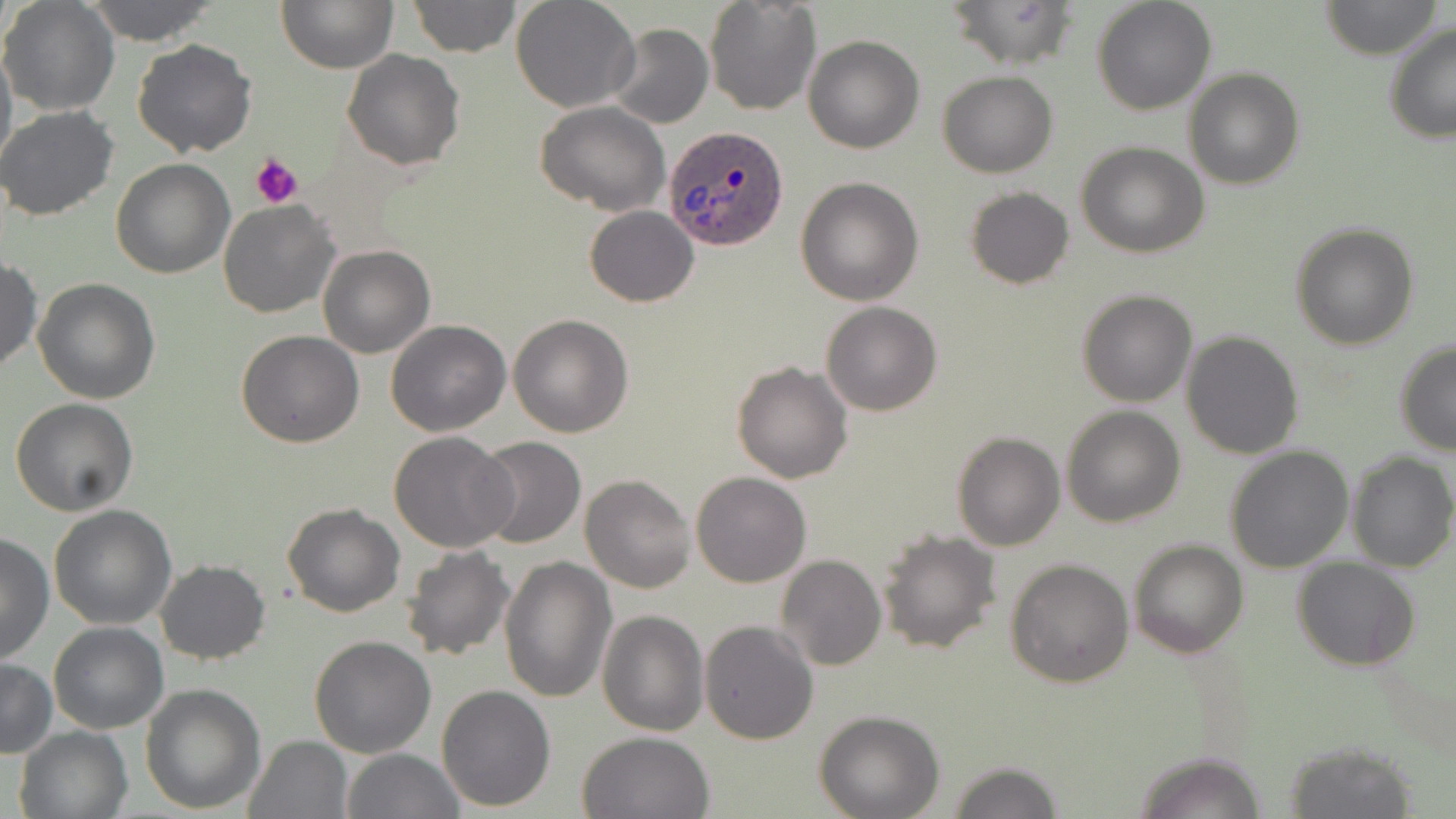
Approximate bounding boxes as (x1,y1)-(x2,y2) corner pairs in pixels. Plasmodium ovale-infected red blood cell locations: (663,123)-(790,250). Uninfected red blood cell locations: (1,0)-(120,117), (83,0)-(220,46), (279,0)-(397,72), (510,0)-(639,113), (704,0)-(822,117), (945,0)-(1079,71), (1091,0)-(1216,115), (407,1)-(521,57), (1321,1)-(1443,58), (1384,21)-(1456,144), (605,23)-(713,129), (0,34)-(16,174), (804,35)-(925,154), (132,38)-(256,156), (342,49)-(466,170), (1183,68)-(1304,189), (938,70)-(1056,177), (536,101)-(670,214), (0,106)-(121,221), (1076,141)-(1209,257), (110,157)-(234,278), (795,176)-(925,305), (965,187)-(1073,290), (219,200)-(339,318), (584,206)-(699,307), (1290,223)-(1420,350), (317,245)-(435,359), (0,255)-(42,372), (32,278)-(160,405), (1077,288)-(1198,406), (821,301)-(942,416), (508,314)-(634,438), (386,320)-(511,437), (236,329)-(364,447), (1181,331)-(1303,460), (1394,342)-(1456,457), (732,361)-(853,483), (11,398)-(139,516), (1061,406)-(1186,527), (388,431)-(516,553), (951,431)-(1065,551), (474,437)-(587,549), (1225,446)-(1353,574), (1346,452)-(1456,572), (690,471)-(812,588), (580,473)-(696,593), (282,501)-(405,617), (49,505)-(177,630), (876,528)-(1001,655), (0,532)-(54,667), (1127,538)-(1249,658), (398,545)-(517,662), (1006,546)-(1251,668), (775,555)-(886,672), (499,557)-(616,705), (1004,558)-(1134,688), (1292,558)-(1422,671), (155,560)-(270,663), (597,608)-(708,736), (699,619)-(818,743), (47,622)-(168,734), (309,634)-(437,757), (1,657)-(56,757), (140,682)-(267,814), (436,684)-(557,811), (815,710)-(945,819), (13,725)-(133,819), (576,730)-(714,818), (243,735)-(354,819), (1281,739)-(1418,818), (343,747)-(466,819), (1133,750)-(1267,819), (946,760)-(1064,818). Platelet locations: (251,153)-(305,209). Slide-level diagnosis: Plasmodium ovale. Single field of view. 1000x magnification. Thin blood smear. May-Grünwald-Giemsa-stained preparation. Image is 1456×819 pixels. Light microscopy.